Name the cell type shown.
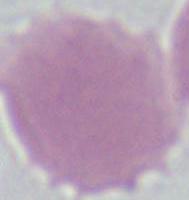
An erythrocyte.

modality = micrograph
magnification = 1000x